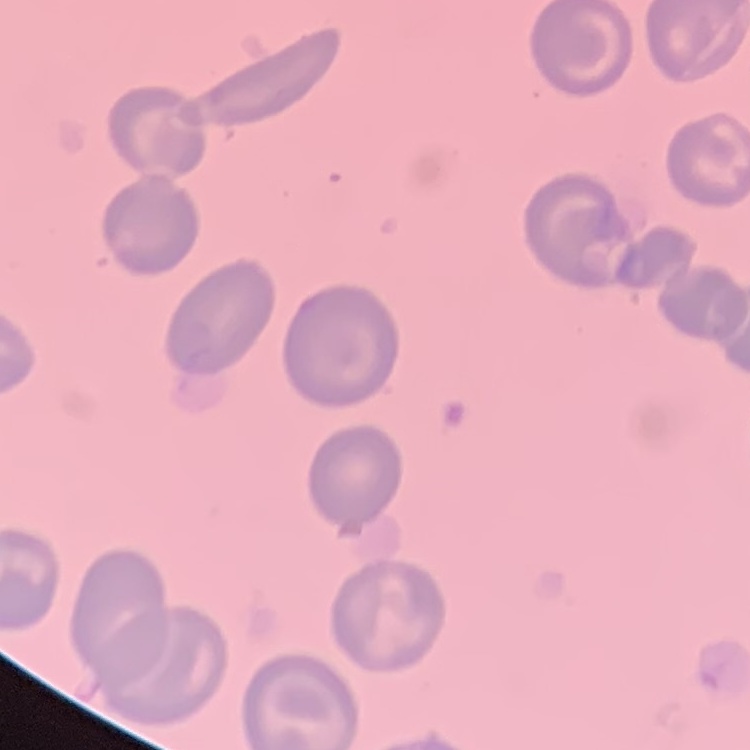

Summary:
  - Red blood cell morphology: no rouleaux formation
  - Image type: square crop of a larger photomicrograph
  - Stain: Field's or Giemsa
  - Preparation: thin blood film